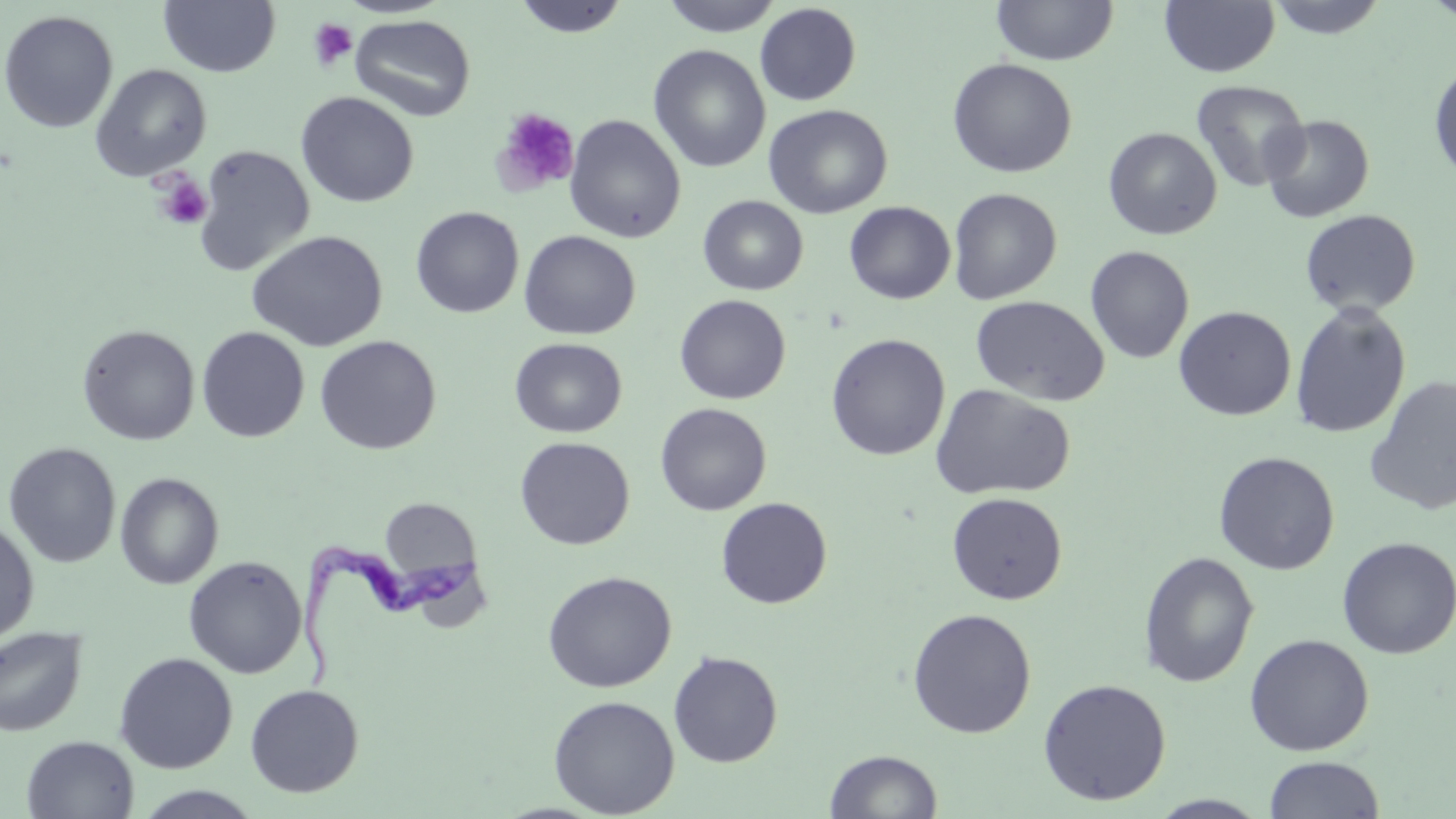
slide-level diagnosis = Trypanosoma brucei
field of view = one of a larger specimen
magnification = 1000x
uninfected red blood cell locations = approximate bounding boxes as named x1/y1/x2/y2 corners in pixels: (x1=159, y1=0, x2=280, y2=77), (x1=514, y1=0, x2=629, y2=38), (x1=660, y1=0, x2=784, y2=37), (x1=992, y1=0, x2=1118, y2=66), (x1=1160, y1=0, x2=1280, y2=77), (x1=1264, y1=0, x2=1390, y2=40), (x1=754, y1=3, x2=861, y2=106), (x1=0, y1=10, x2=119, y2=132), (x1=350, y1=14, x2=476, y2=122), (x1=648, y1=45, x2=770, y2=173), (x1=947, y1=58, x2=1077, y2=178), (x1=1428, y1=59, x2=1456, y2=186), (x1=90, y1=64, x2=212, y2=180), (x1=1191, y1=80, x2=1310, y2=192), (x1=296, y1=91, x2=419, y2=208), (x1=763, y1=104, x2=893, y2=219), (x1=564, y1=114, x2=687, y2=243), (x1=1261, y1=115, x2=1374, y2=223), (x1=1102, y1=127, x2=1222, y2=240), (x1=193, y1=145, x2=315, y2=276), (x1=948, y1=187, x2=1062, y2=305), (x1=698, y1=195, x2=808, y2=295), (x1=844, y1=201, x2=955, y2=304), (x1=410, y1=206, x2=524, y2=318), (x1=1299, y1=209, x2=1421, y2=317), (x1=247, y1=230, x2=388, y2=352), (x1=520, y1=230, x2=641, y2=340), (x1=1085, y1=245, x2=1195, y2=364), (x1=674, y1=294, x2=791, y2=404), (x1=970, y1=296, x2=1109, y2=406), (x1=1289, y1=302, x2=1412, y2=439), (x1=1173, y1=306, x2=1296, y2=421), (x1=77, y1=324, x2=200, y2=445), (x1=196, y1=326, x2=310, y2=443), (x1=826, y1=333, x2=950, y2=461), (x1=314, y1=335, x2=442, y2=455), (x1=510, y1=337, x2=627, y2=438), (x1=1364, y1=376, x2=1456, y2=515), (x1=930, y1=383, x2=1076, y2=501), (x1=655, y1=403, x2=772, y2=516), (x1=515, y1=436, x2=635, y2=550), (x1=3, y1=442, x2=121, y2=568), (x1=1214, y1=451, x2=1340, y2=575), (x1=115, y1=472, x2=224, y2=589), (x1=946, y1=492, x2=1068, y2=605), (x1=379, y1=497, x2=482, y2=584), (x1=716, y1=497, x2=833, y2=609), (x1=0, y1=516, x2=39, y2=647), (x1=1337, y1=536, x2=1456, y2=659), (x1=1138, y1=551, x2=1259, y2=688), (x1=183, y1=556, x2=307, y2=679), (x1=542, y1=570, x2=677, y2=692), (x1=907, y1=608, x2=1037, y2=739), (x1=0, y1=626, x2=88, y2=737), (x1=1244, y1=633, x2=1374, y2=756), (x1=668, y1=650, x2=783, y2=768), (x1=113, y1=652, x2=238, y2=774), (x1=1037, y1=678, x2=1172, y2=806), (x1=245, y1=684, x2=364, y2=797), (x1=548, y1=694, x2=680, y2=817), (x1=21, y1=735, x2=139, y2=818), (x1=825, y1=749, x2=943, y2=819), (x1=1263, y1=755, x2=1385, y2=818), (x1=133, y1=786, x2=264, y2=818), (x1=1148, y1=794, x2=1272, y2=818)
stain = May-Grünwald-Giemsa
image size = 1456×819 pixels
Trypanosoma brucei locations = approximate bounding boxes as named x1/y1/x2/y2 corners in pixels: (x1=296, y1=538, x2=482, y2=693)
platelet locations = approximate bounding boxes as named x1/y1/x2/y2 corners in pixels: (x1=308, y1=17, x2=358, y2=72), (x1=492, y1=107, x2=581, y2=195), (x1=152, y1=172, x2=213, y2=230)
modality = light microscopy
preparation = thin blood smear